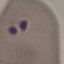

Malaria status: parasitized. Giemsa stain. Thin blood film. Photographed with a smartphone camera at the microscope eyepiece. Automatically extracted cell patch, resized to 64 × 64 pixels.